Describe the morphology of the erythrocytes.
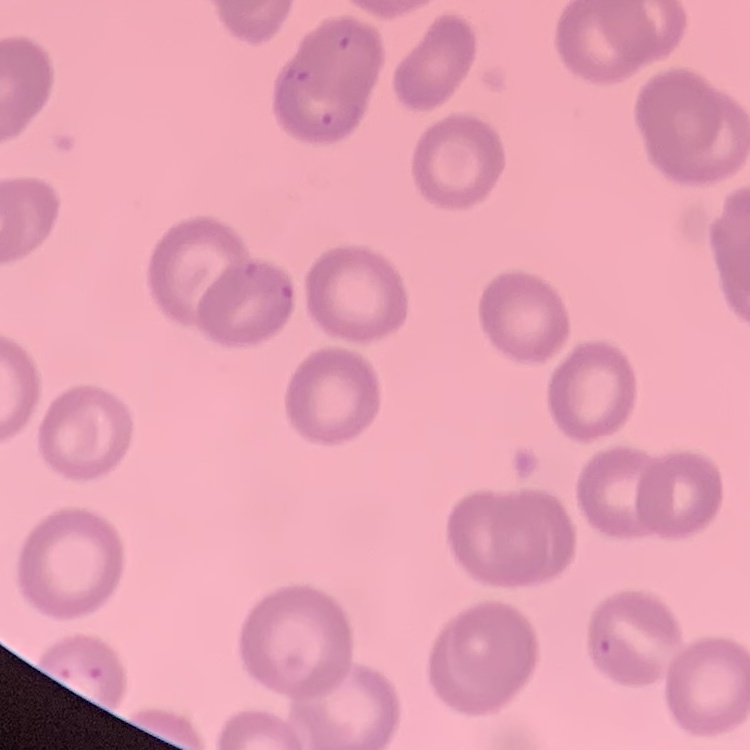

No rouleaux formation.

Summary:
  - Preparation: thin blood film
  - Stain: Field's or Giemsa
  - Image type: one tile cut from a larger photomicrograph